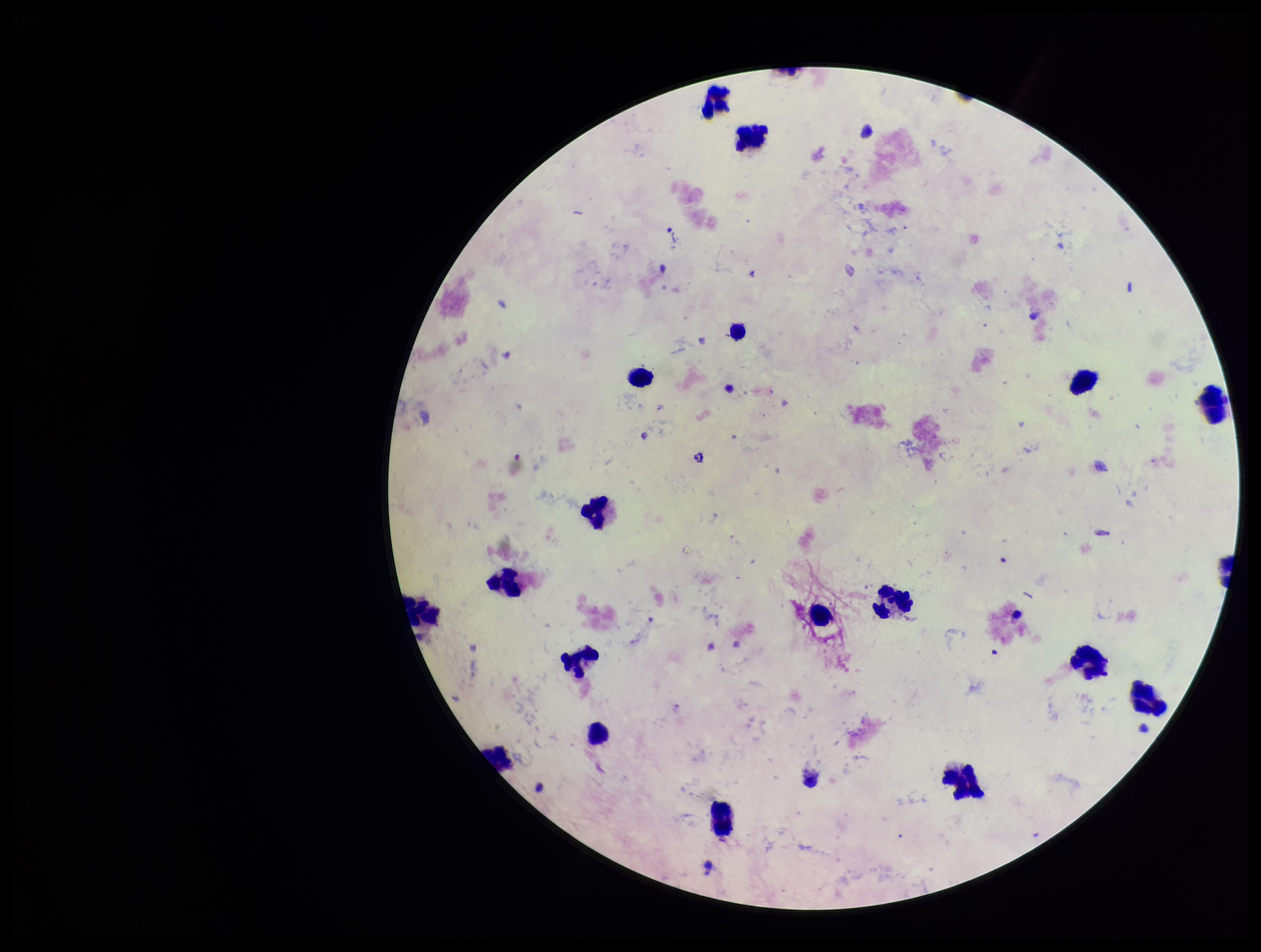
Summary:
  - Patient malaria status: negative
  - Preparation: thick
  - Plasmodium parasites: none seen
  - Stain: Giemsa
  - Parasite count: 0
  - Field of view: single
  - Capture: smartphone photograph through the microscope eyepiece
  - Leukocyte count: 18
  - Image size: 1261×952 pixels